Give the extent of all Trypanosoma brucei.
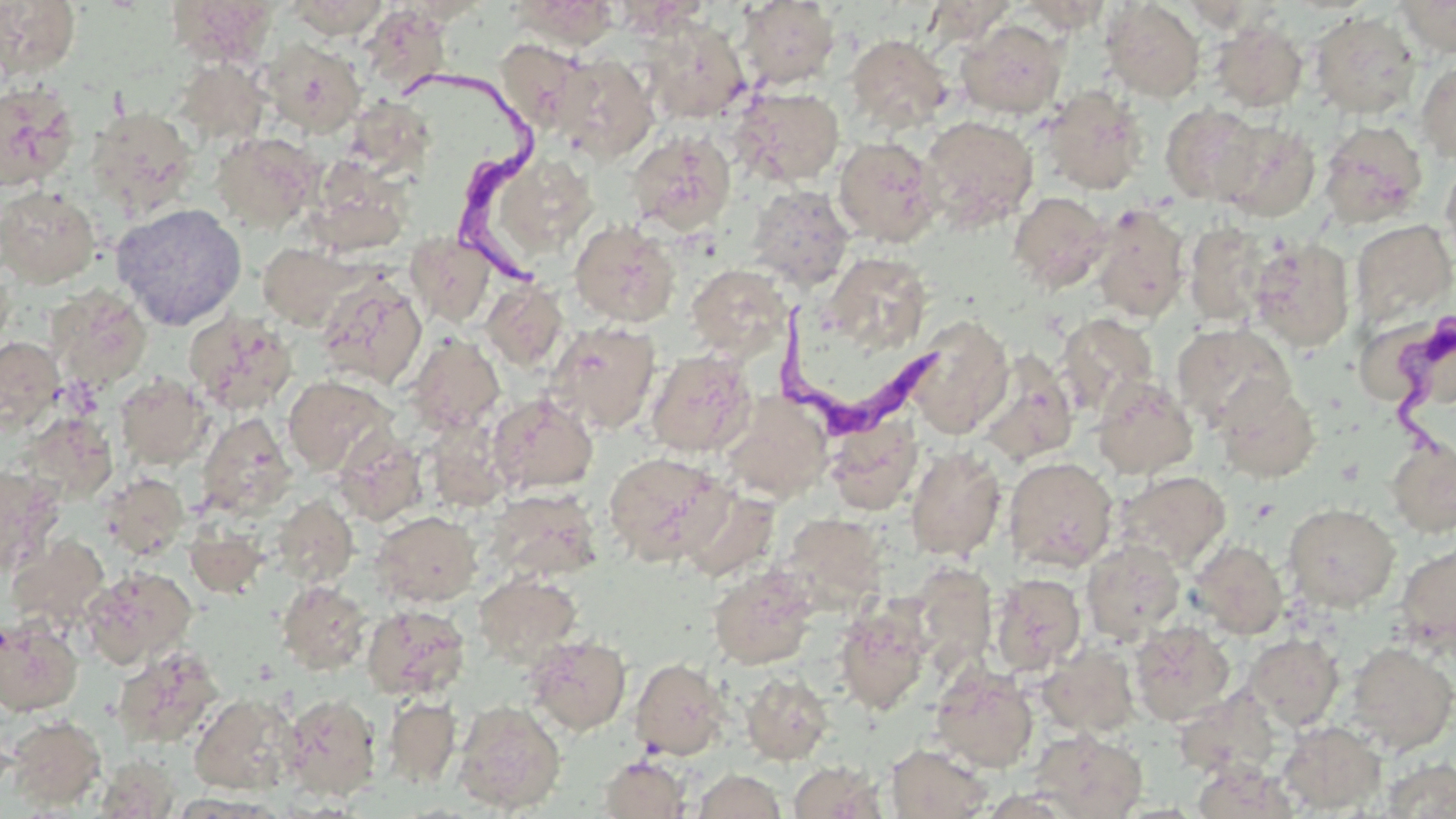

Approximate bounding boxes as [x1, y1, x2, y2] in pixels.
Trypanosoma brucei: [410, 76, 555, 292], [770, 292, 940, 438], [1380, 318, 1455, 455].

Summary:
  - Uninfected red blood cell locations: [165, 0, 279, 67], [284, 0, 392, 40], [510, 0, 624, 51], [1393, 0, 1456, 58], [0, 1, 81, 80], [737, 1, 840, 90], [922, 1, 1020, 47], [1015, 1, 1112, 33], [1100, 1, 1205, 102], [360, 5, 454, 97], [1310, 10, 1421, 119], [644, 17, 750, 124], [956, 18, 1067, 119], [1210, 20, 1308, 113], [846, 34, 952, 133], [261, 37, 366, 136], [495, 39, 586, 133], [552, 54, 658, 164], [173, 58, 270, 146], [1415, 59, 1456, 163], [0, 82, 79, 192], [1040, 85, 1147, 195], [731, 86, 845, 187], [345, 98, 435, 176], [1160, 104, 1268, 206], [85, 106, 198, 220], [919, 115, 1039, 233], [1213, 120, 1321, 222], [1319, 120, 1428, 228], [211, 130, 322, 232], [626, 130, 736, 235], [833, 136, 942, 247], [483, 151, 600, 263], [1440, 155, 1456, 267], [305, 156, 411, 256], [746, 185, 854, 291], [0, 186, 101, 288], [1008, 191, 1112, 292], [110, 203, 248, 331], [1090, 203, 1190, 323], [1349, 218, 1456, 327], [569, 219, 680, 328], [1184, 221, 1270, 325], [405, 232, 496, 327], [1248, 238, 1356, 352], [258, 242, 362, 329], [822, 251, 933, 352], [686, 263, 791, 359], [316, 274, 428, 390], [481, 280, 568, 372], [46, 286, 153, 391], [184, 309, 298, 415], [1056, 313, 1158, 416], [905, 315, 1013, 438], [546, 321, 661, 434], [1171, 322, 1294, 433], [405, 333, 505, 434], [0, 337, 64, 433], [646, 349, 757, 457], [976, 349, 1079, 467], [115, 373, 212, 468], [283, 376, 394, 475], [1091, 376, 1198, 480], [1213, 379, 1321, 483], [488, 393, 599, 494], [719, 393, 832, 502], [196, 413, 297, 519], [825, 415, 923, 515], [424, 418, 513, 513], [333, 430, 428, 526], [1387, 436, 1455, 538], [905, 445, 1006, 561], [603, 452, 730, 567], [1003, 456, 1118, 572], [0, 466, 62, 577], [1115, 470, 1231, 572], [100, 473, 189, 559], [678, 486, 780, 582], [485, 488, 602, 584], [272, 495, 358, 588], [1283, 503, 1400, 611], [371, 510, 482, 607], [780, 513, 888, 610], [185, 525, 268, 597], [6, 535, 109, 629], [1081, 539, 1185, 644], [1189, 539, 1288, 638], [1395, 541, 1456, 653], [909, 562, 998, 675], [708, 565, 818, 671], [81, 566, 197, 668], [473, 572, 582, 667], [990, 573, 1086, 676], [277, 580, 372, 675], [833, 602, 932, 715], [362, 604, 470, 701], [0, 617, 83, 716], [2, 618, 93, 811], [1130, 621, 1235, 725], [1245, 633, 1344, 729], [525, 635, 632, 735], [1343, 641, 1456, 755], [1036, 645, 1139, 737], [113, 646, 224, 749], [629, 657, 731, 761], [931, 665, 1039, 773], [740, 672, 833, 766], [1174, 689, 1278, 778], [281, 692, 382, 801], [189, 693, 298, 795], [383, 696, 461, 787], [453, 700, 566, 814], [4, 715, 106, 810], [1278, 720, 1385, 814], [1030, 729, 1147, 819], [887, 743, 993, 818], [96, 754, 179, 818], [598, 755, 691, 818], [1379, 759, 1455, 818], [788, 762, 885, 819], [1191, 762, 1301, 817], [693, 769, 785, 818]
  - Slide-level diagnosis: Trypanosoma brucei
  - Field of view: one of a larger specimen
  - Image size: 1456×819 pixels
  - Magnification: 1000x
  - Stain: May-Grünwald-Giemsa
  - Preparation: thin blood film
  - Modality: light microscopy